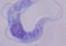

Summary:
  - Modality: photomicrograph
  - Magnification: 1000x
  - Identification: trypanosome